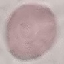

malaria status = uninfected
preparation = thin blood smear
stain = Giemsa
capture = smartphone camera at the microscope eyepiece
image type = cell patch, automatically extracted from a larger field of view and resized to 64 × 64 pixels